Assess this cell for malaria.
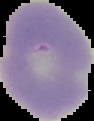
It is uninfected.

Cell region segmented out of the field of view; the surrounding area is masked to black. Image is 94×121 pixels. From a thin blood smear.